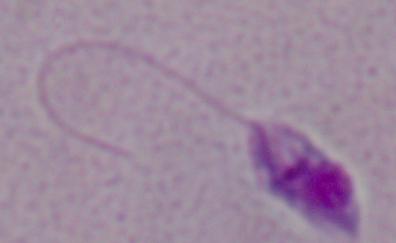
Summary:
  - Magnification: 1000x
  - Identification: Leishmania
  - Modality: photomicrograph